Classify this cell by malaria status.
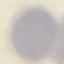

It is uninfected.

Summary:
  - Stain: Giemsa
  - Capture: smartphone camera at the microscope eyepiece
  - Preparation: thin smear
  - Image type: cell patch, automatically extracted from a larger field of view and resized to 64 × 64 pixels